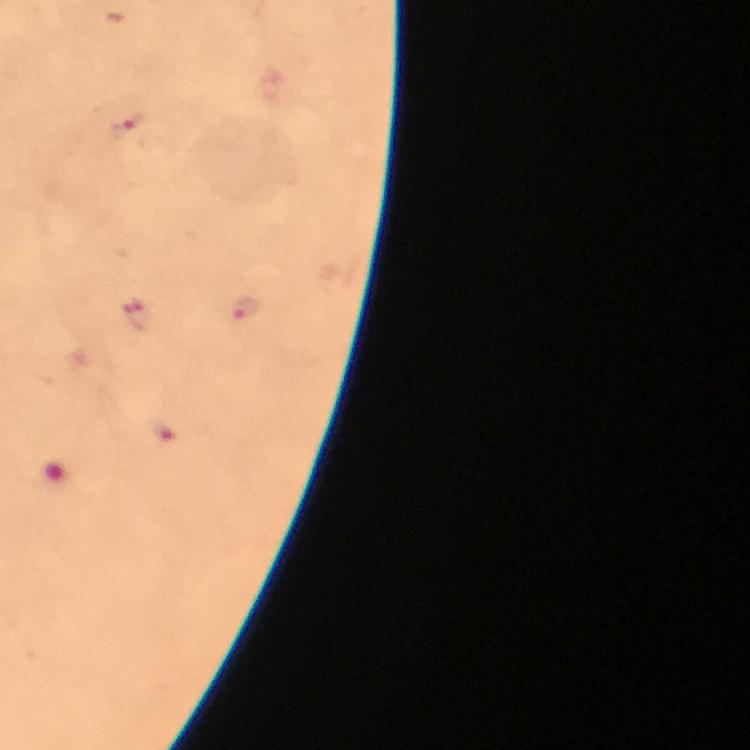

Approximate centers as {x, y} in pixels.
Summary:
  - Plasmodium parasite locations: {131, 131}, {244, 307}, {139, 316}, {165, 430}
  - Preparation: thick blood smear
  - Context: from a malaria diagnostic workup
  - Immersion oil: used
  - Capture: smartphone mounted on the microscope
  - Cropped from: one field of view
  - Magnification: 100x
  - Image size: 750×750 pixels
  - Stain: Giemsa